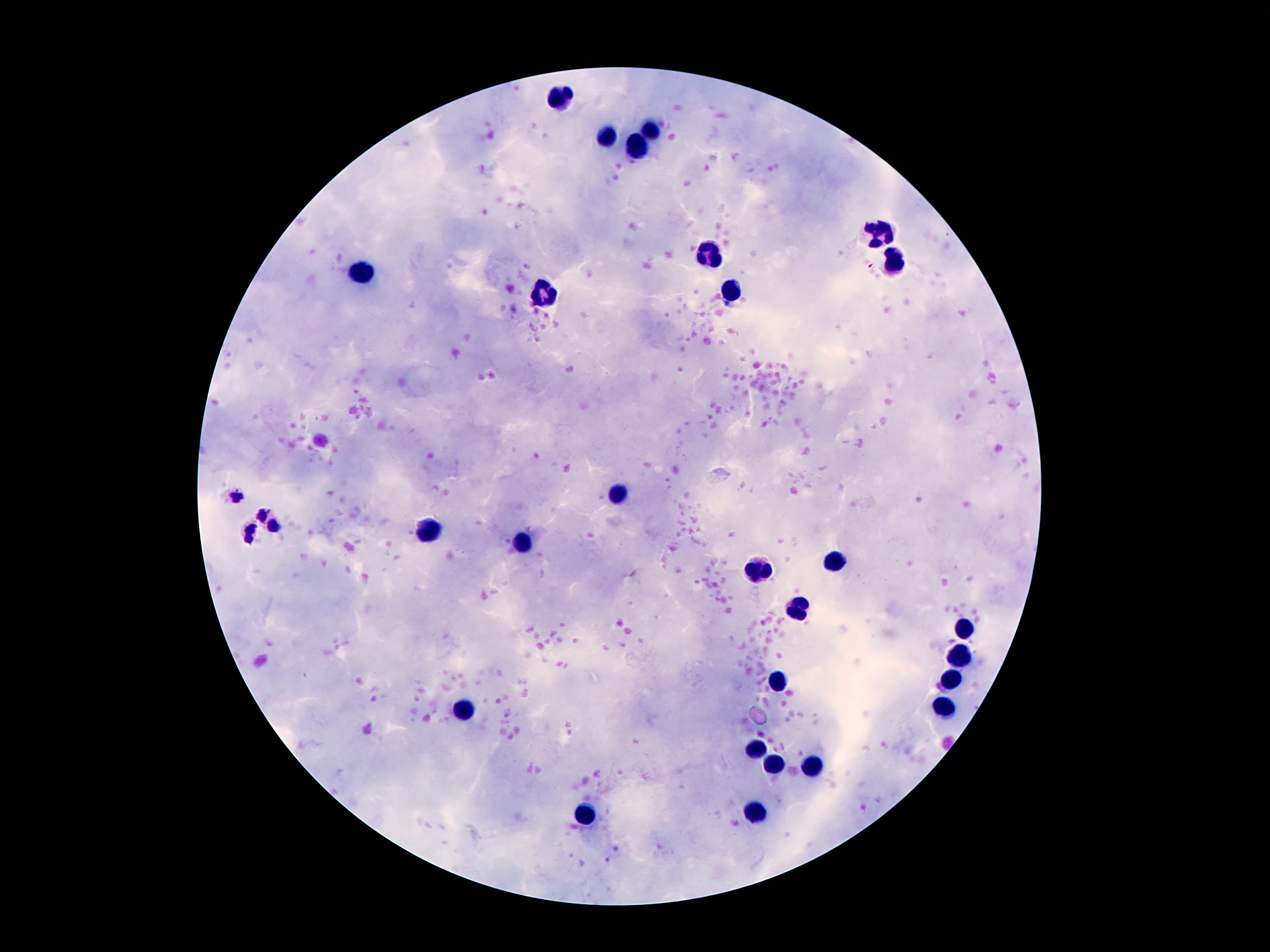
Approximate object centers, in pixels from the top-left corner. Leukocyte locations: (x=558, y=96), (x=652, y=131), (x=611, y=135), (x=637, y=147), (x=881, y=234), (x=713, y=254), (x=896, y=262), (x=364, y=271), (x=547, y=292), (x=730, y=294), (x=618, y=494), (x=428, y=529), (x=525, y=544), (x=833, y=559), (x=752, y=567), (x=799, y=611), (x=967, y=630), (x=958, y=657), (x=950, y=678), (x=779, y=684), (x=943, y=704), (x=463, y=712), (x=756, y=751), (x=775, y=766), (x=812, y=766), (x=756, y=809), (x=588, y=813). Giemsa stain. Photographed through the microscope eyepiece with a smartphone camera. One field from this slide. 100x magnification. Thick blood film. Image is 1270×952 pixels. Patient malaria status: uninfected.